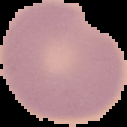
From a thin blood film. Image is 127×127 pixels. Malaria status: uninfected. Cell region segmented out of the field of view; the surrounding area is masked to black.